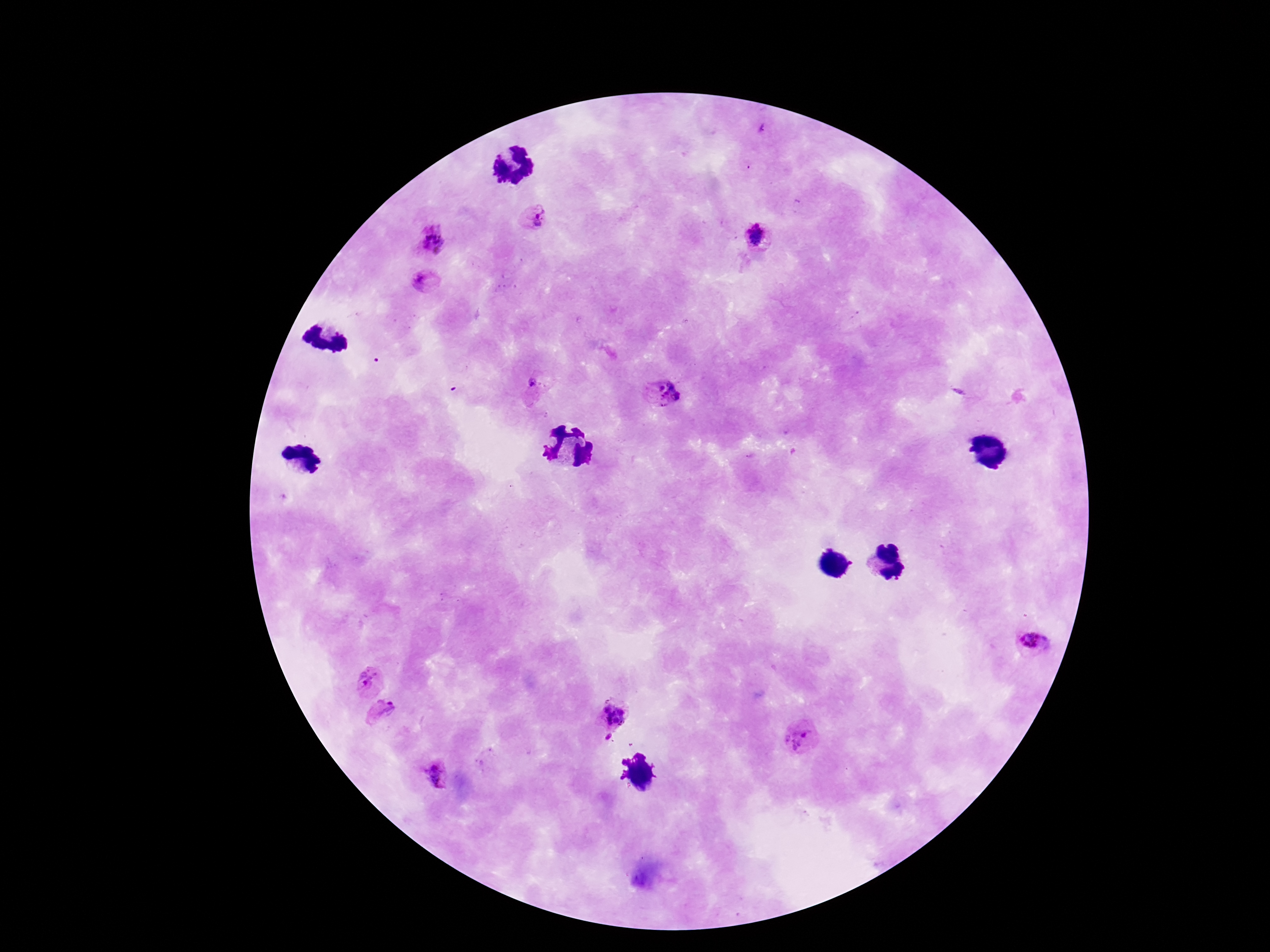

Approximate object centers, in pixels from the top-left corner. Plasmodium parasite locations: (x=763, y=128), (x=536, y=218), (x=757, y=237), (x=431, y=241), (x=424, y=282), (x=535, y=384), (x=663, y=393), (x=1035, y=643), (x=368, y=679), (x=385, y=712), (x=613, y=715), (x=801, y=737), (x=608, y=738), (x=436, y=775). Thick peripheral-blood smear. One field from this slide. Giemsa stain. 100x magnification. Photographed through the microscope eyepiece with a smartphone camera. Image is 1270×952 pixels. Patient malaria status: infected.